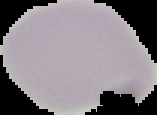
result = no Plasmodium parasites detected
image size = 157×115 pixels
image type = cell region segmented out of the field of view; surrounding area masked to black
preparation = thin blood smear